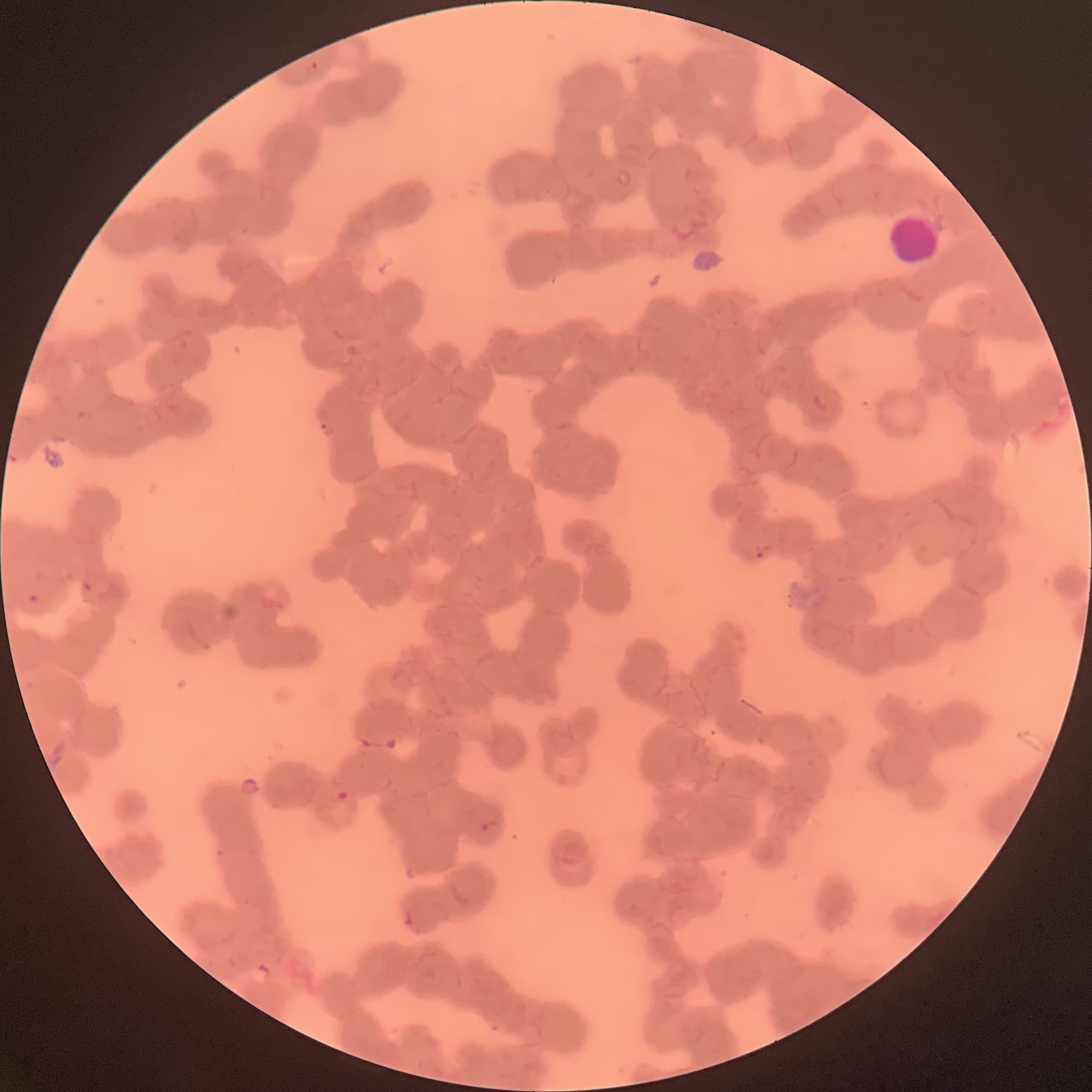
coordinate format = approximate bounding boxes as (x1, y1, x2, y2) in pixels
white blood cell locations = (885, 211, 942, 267)
Plasmodium parasite locations = (304, 60, 319, 79), (317, 421, 335, 438), (754, 542, 771, 561), (81, 580, 93, 593), (27, 593, 41, 604), (335, 791, 359, 811), (481, 819, 500, 833), (400, 909, 418, 931)
image size = 1092×1092 pixels
red blood cell morphology = rouleaux formation
modality = light microscopy
preparation = thin blood film